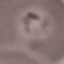
result = malaria parasites identified
preparation = thin blood smear
capture = smartphone through the microscope eyepiece
stain = Giemsa
image type = automatically extracted cell patch, resized to 64 × 64 pixels